State the preparation type.
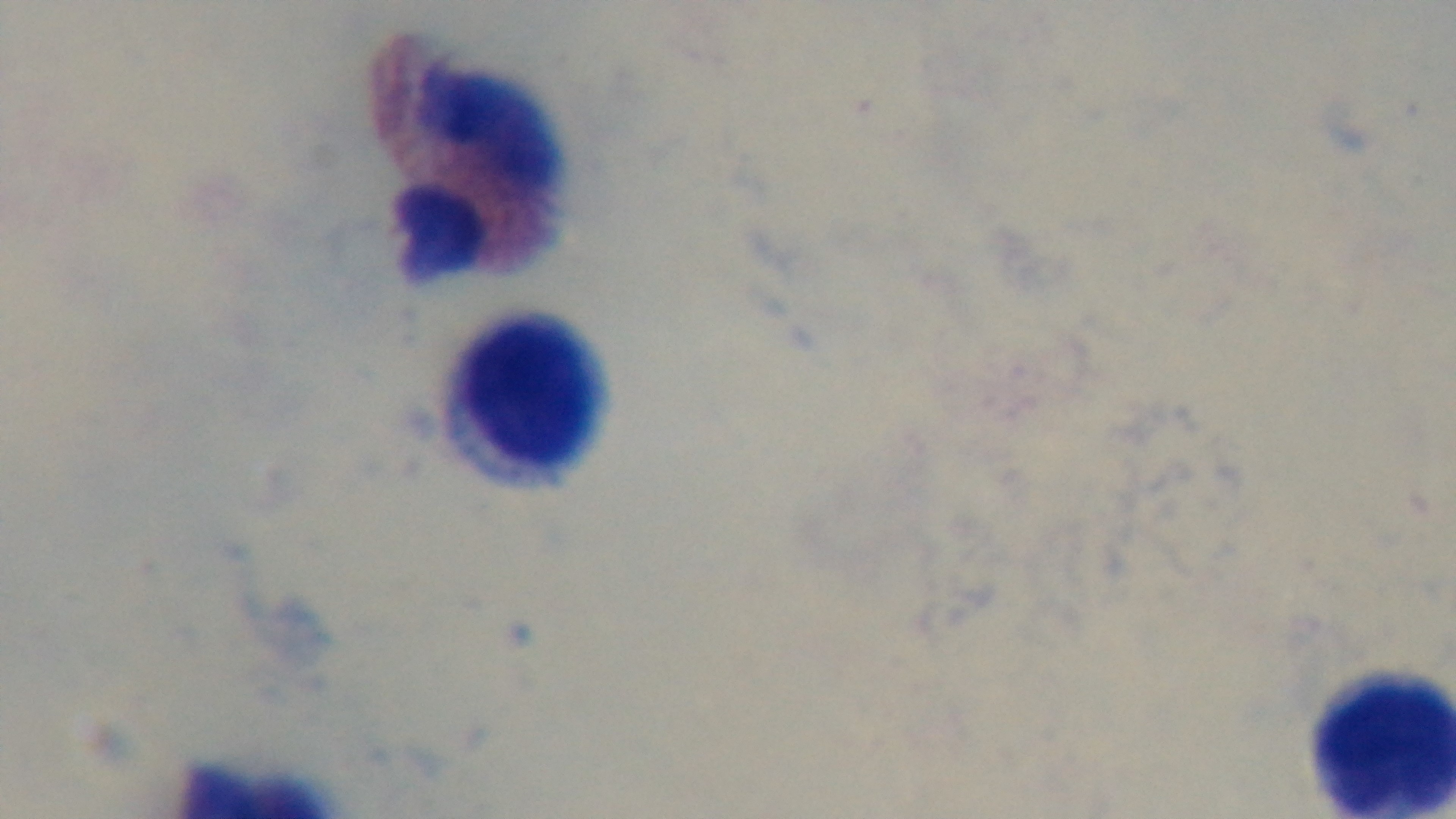

It is a thick blood film.

stain: Giemsa
objective: 100x oil immersion
modality: light microscopy
capture: mounted 4K digital camera
malaria_status: uninfected
field_of_view: one from the slide